State the blood parasite species.
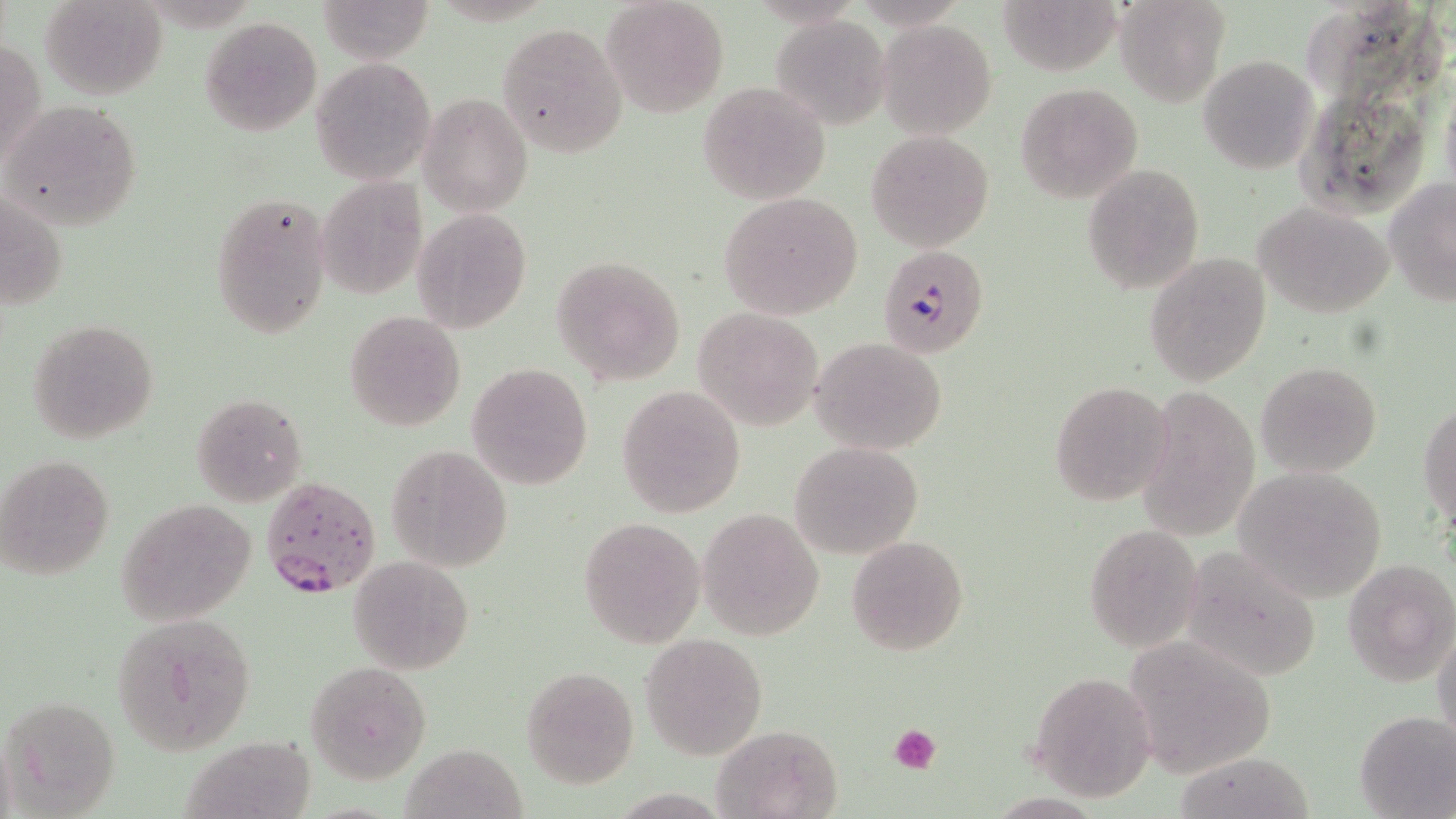

Plasmodium falciparum.

Summary:
  - Coordinate format: approximate bounding boxes as (x1, y1, x2, y2) in pixels
  - Uninfected red blood cell locations: (41, 0, 167, 101), (316, 0, 435, 65), (601, 0, 728, 119), (1113, 0, 1230, 107), (1003, 1, 1126, 78), (199, 16, 323, 136), (771, 16, 891, 129), (878, 21, 997, 138), (498, 22, 626, 160), (1, 35, 45, 169), (1198, 55, 1318, 174), (310, 57, 435, 184), (697, 81, 832, 205), (1016, 82, 1144, 202), (419, 92, 534, 217), (3, 100, 143, 229), (866, 130, 993, 251), (1083, 164, 1204, 293), (1385, 177, 1456, 307), (317, 178, 427, 299), (2, 191, 68, 312), (210, 191, 331, 337), (717, 192, 864, 318), (1255, 201, 1395, 317), (413, 208, 530, 334), (1145, 252, 1271, 388), (553, 255, 687, 385), (691, 307, 825, 430), (345, 311, 466, 431), (28, 317, 161, 445), (810, 337, 949, 456), (1256, 361, 1382, 476), (468, 363, 593, 490), (1050, 381, 1175, 504), (1133, 383, 1261, 544), (616, 385, 746, 517), (190, 393, 307, 506), (1420, 400, 1455, 527), (791, 442, 922, 559), (386, 444, 512, 571), (1, 455, 114, 579), (1232, 465, 1390, 600), (117, 498, 257, 625), (696, 509, 825, 640), (579, 516, 705, 650), (1084, 524, 1203, 649), (845, 534, 968, 657), (1179, 546, 1324, 681), (348, 555, 475, 674), (1342, 556, 1455, 689), (113, 614, 257, 753), (1432, 624, 1456, 750), (1126, 626, 1275, 775), (641, 633, 767, 759), (305, 661, 432, 784), (520, 665, 639, 789), (1027, 674, 1157, 802), (3, 693, 121, 817), (1355, 709, 1455, 818), (710, 724, 841, 818), (180, 729, 314, 819), (399, 744, 524, 817), (1178, 748, 1322, 818)
  - Plasmodium falciparum-infected red blood cell locations: (878, 244, 990, 358), (262, 474, 382, 598)
  - Platelet locations: (888, 723, 943, 774)
  - Image size: 1456×819 pixels
  - Modality: light microscopy
  - Stain: May-Grünwald-Giemsa
  - Field of view: single
  - Magnification: 1000x
  - Preparation: thin blood film